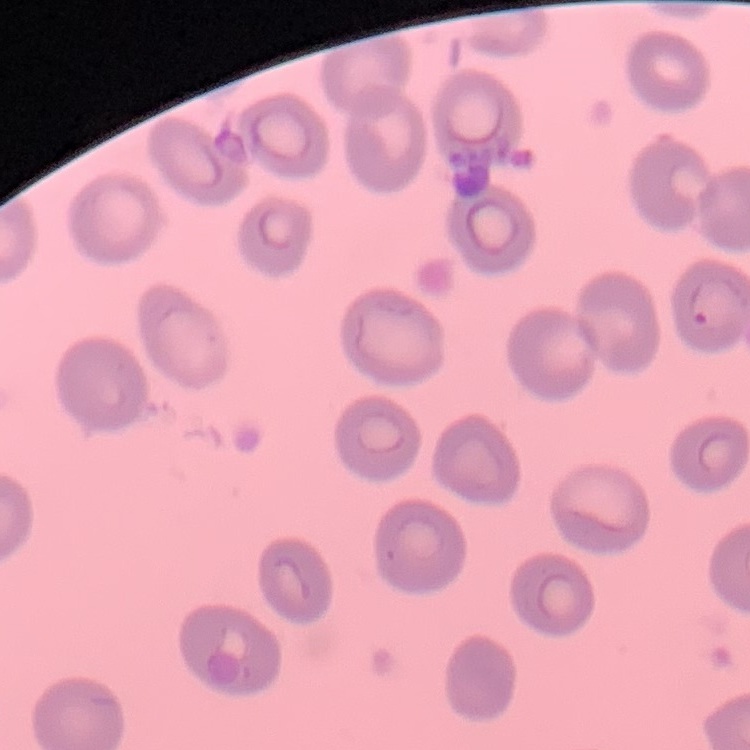

The red blood cells exhibit no rouleaux formation. Square crop of a larger photomicrograph. Thin blood smear. Stained with either Field's or Giemsa.